Identify the preparation type.
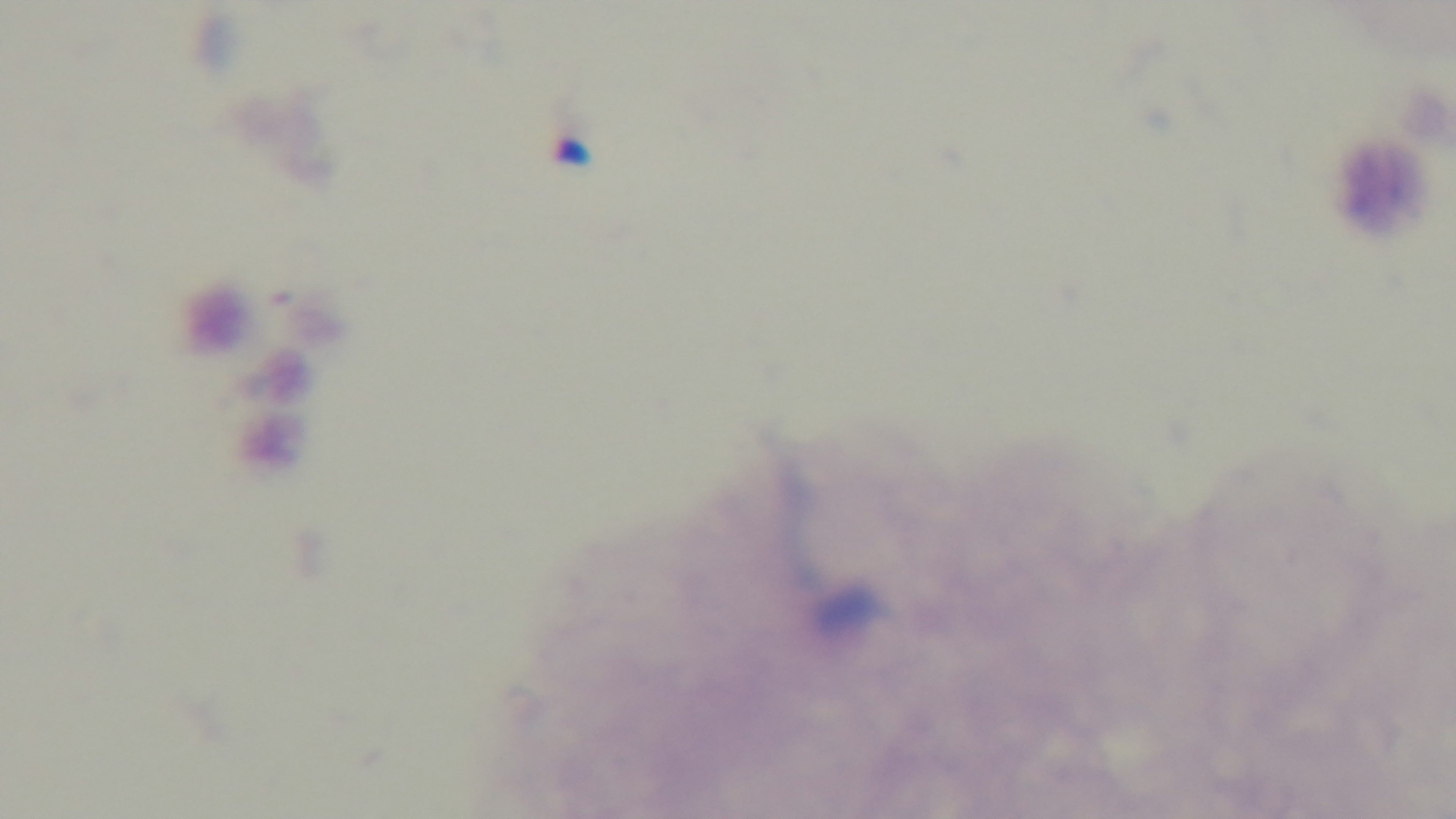
A thick smear.

Summary:
  - Capture: mounted 4K digital camera
  - Malaria status: negative
  - Objective: 100x oil immersion
  - Modality: light microscopy
  - Field of view: single
  - Stain: Giemsa